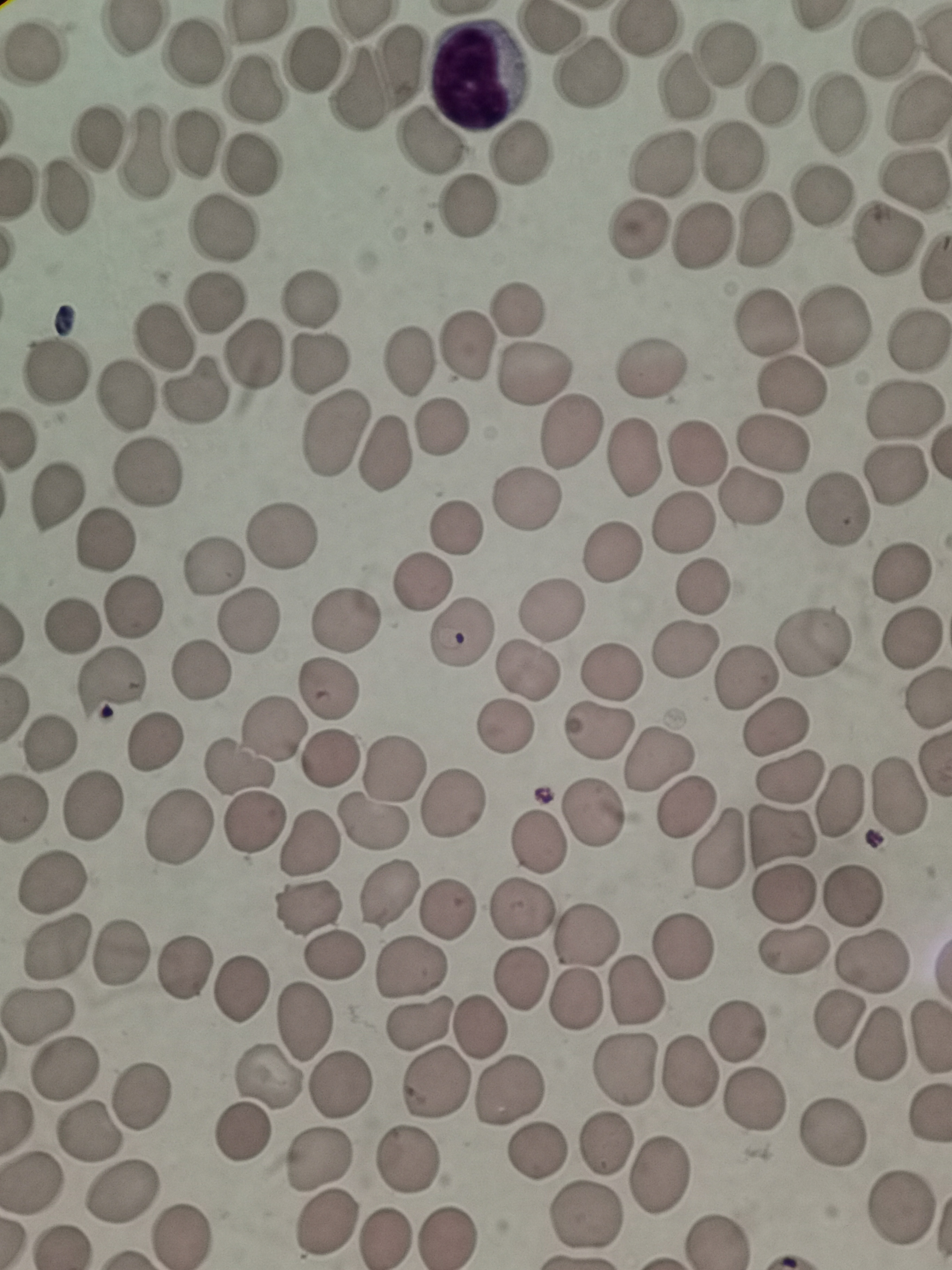
{
  "cell_locations": "approximate centers as {x, y} in pixels: {883, 44}, {719, 50}, {188, 52}, {309, 61}, {588, 71}, {357, 87}, {255, 88}, {680, 88}, {770, 94}, {917, 107}, {837, 115}, {101, 138}, {431, 142}, {199, 143}, {731, 152}, {139, 154}, {516, 157}, {248, 162}, {662, 162}, {910, 179}, {65, 195}, {822, 198}, {464, 208}, {225, 224}, {639, 225}, {763, 228}, {701, 234}, {885, 235}, {215, 300}, {307, 302}, {518, 310}, {765, 322}, {836, 326}, {160, 338}, {915, 338}, {464, 347}, {252, 354}, {409, 359}, {317, 362}, {649, 369}, {533, 373}, {58, 377}, {789, 383}, {194, 390}, {123, 396}, {903, 412}, {440, 425}, {571, 431}, {333, 433}, {771, 444}, {384, 452}, {634, 455}, {698, 455}, {894, 471}, {146, 472}, {749, 499}, {525, 500}, {54, 501}, {837, 510}, {683, 520}, {455, 530}, {278, 537}, {104, 544}, {614, 552}, {212, 566}, {898, 573}, {423, 583}, {702, 586}, {128, 607}, {552, 608}, {344, 618}, {248, 619}, {73, 630}, {464, 632}, {910, 641}, {811, 643}, {687, 646}, {527, 669}, {610, 671}, {200, 674}, {112, 683}, {747, 683}, {328, 691}, {504, 725}, {777, 728}, {599, 729}, {274, 731}, {155, 742}, {50, 744}, {660, 758}, {331, 759}, {240, 769}, {391, 773}, {791, 779}, {897, 792}, {837, 801}, {454, 802}, {92, 807}, {687, 807}, {595, 813}, {377, 821}, {181, 824}, {252, 825}, {783, 838}, {539, 843}, {306, 846}, {716, 849}, {52, 888}, {389, 891}, {784, 892}, {852, 897}, {443, 908}, {306, 909}, {522, 911}, {586, 934}, {685, 946}, {58, 947}, {795, 947}, {120, 953}, {334, 953}, {874, 959}, {412, 967}, {183, 968}, {521, 978}, {635, 988}, {239, 991}, {572, 999}, {834, 1017}, {38, 1018}, {304, 1019}, {419, 1021}, {479, 1029}, {738, 1030}, {880, 1042}, {690, 1070}, {622, 1071}, {68, 1072}, {436, 1081}, {264, 1082}, {338, 1083}, {509, 1089}, {142, 1094}, {758, 1100}, {88, 1132}, {242, 1132}, {832, 1132}, {605, 1145}, {533, 1149}, {318, 1157}, {406, 1159}, {656, 1172}, {32, 1183}, {123, 1189}, {900, 1209}, {588, 1213}, {326, 1224}, {449, 1234}, {184, 1235}, {388, 1237}, {715, 1237}",
  "capture": "smartphone through the microscope eyepiece",
  "field_of_view": "single",
  "stain": "Giemsa",
  "image_size": "952×1270 pixels",
  "preparation": "thin blood film"
}